State which parasite is depicted.
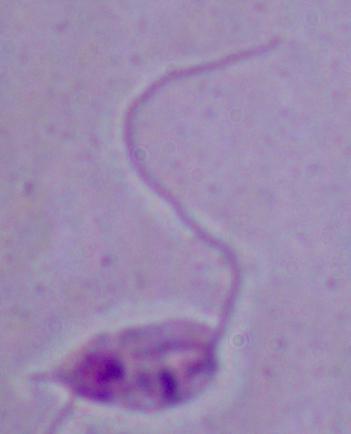

This is Leishmania.

{
  "magnification": "1000x",
  "modality": "photomicrograph"
}